Report the malaria status of this cell.
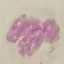
It is uninfected.

stain: Giemsa
image_type: cell patch, automatically extracted from a larger field of view and resized to 64 × 64 pixels
capture: smartphone through the microscope eyepiece
preparation: thin blood smear